Assess this cell for malaria.
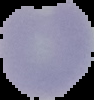
Uninfected.

Summary:
  - Image type: cell region segmented out of the field of view; surrounding area masked to black
  - Image size: 94×100 pixels
  - Preparation: thin blood smear